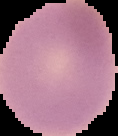

image type = cell region segmented out of the field of view; surrounding area masked to black
preparation = thin blood smear
result = negative for malaria parasites
image size = 118×136 pixels